Comment on the morphology of the erythrocytes.
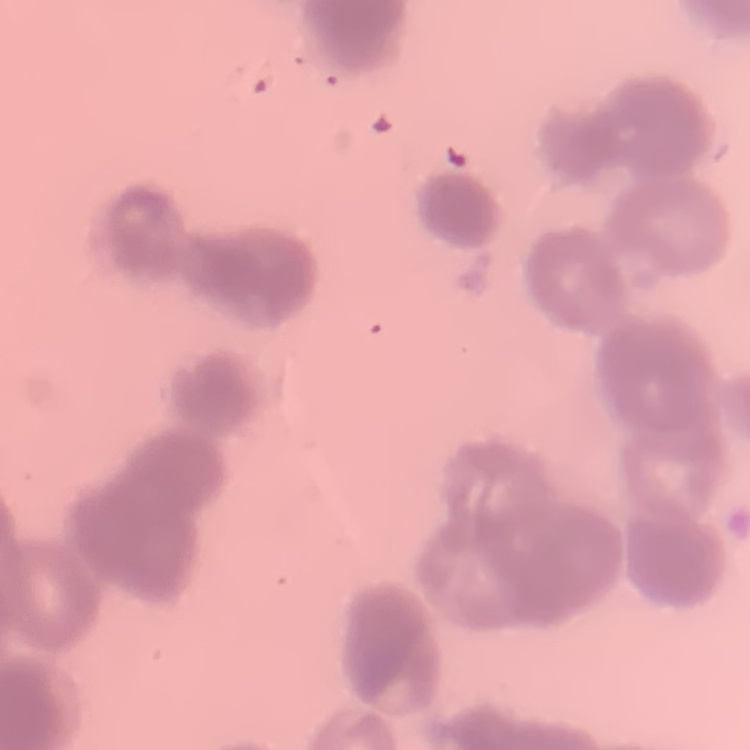
They show rouleaux formation.

Field's or Giemsa stain. Square crop of a larger photomicrograph. Thin peripheral smear.